Report the malaria status of this cell.
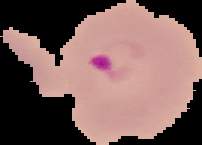
It is parasitized.

Summary:
  - Image size: 202×145 pixels
  - Preparation: thin blood smear
  - Image type: segmented cell region with the area outside set to black